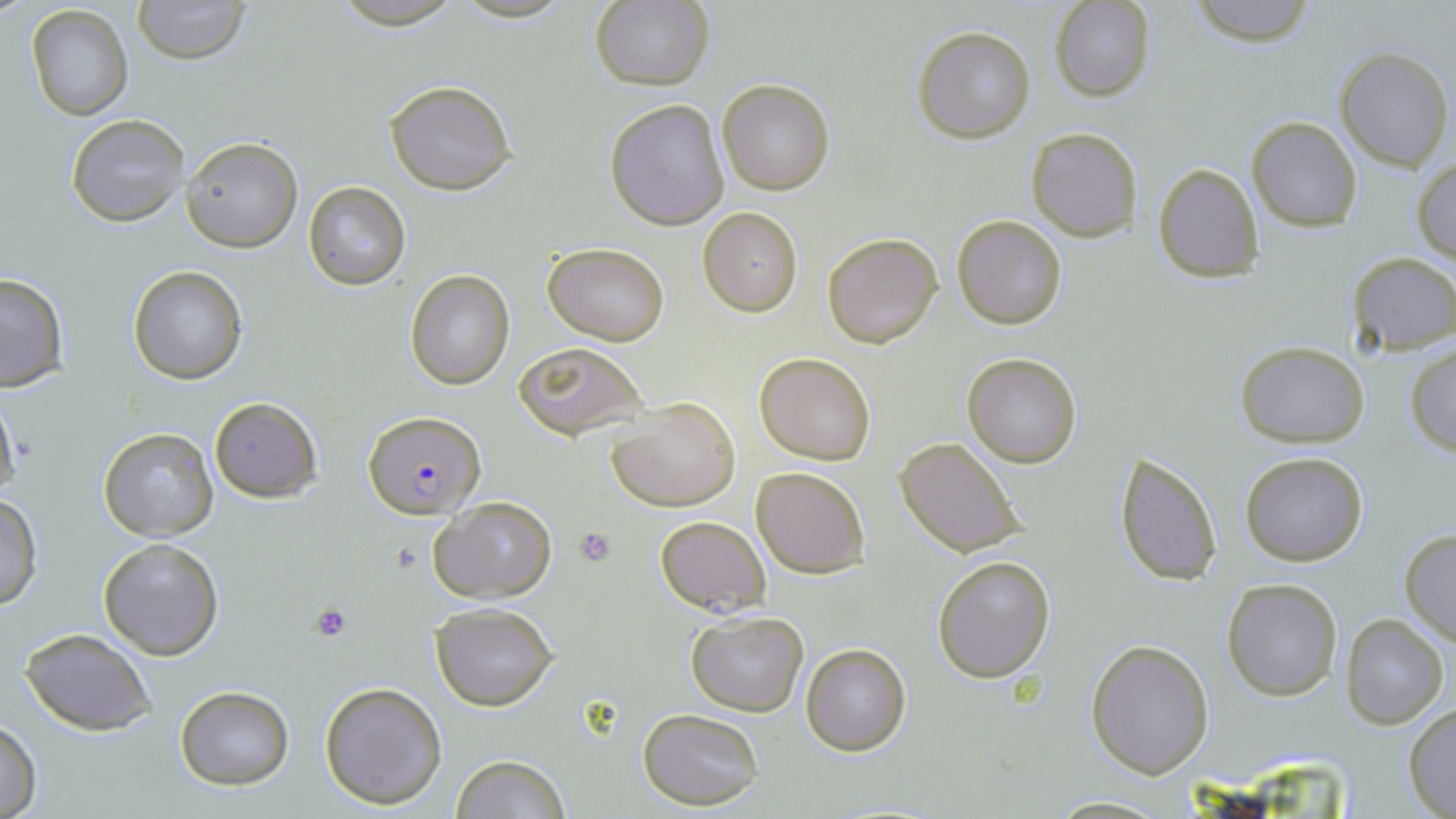

Summary:
  - Coordinate format: approximate bounding boxes as (x1,y1)-(x2,y2) corner pairs in pixels
  - Plasmodium falciparum-infected red blood cell locations: (362,410)-(483,518)
  - Platelet locations: (575,526)-(616,566), (310,603)-(352,642)
  - Uninfected red blood cell locations: (131,0)-(251,64), (329,0)-(465,28), (590,0)-(714,91), (1188,0)-(1319,45), (1050,1)-(1155,102), (26,5)-(132,119), (913,26)-(1037,144), (1333,46)-(1453,171), (383,78)-(517,195), (715,78)-(836,196), (604,99)-(729,230), (66,113)-(188,227), (1246,116)-(1362,232), (1025,127)-(1143,242), (183,137)-(304,253), (1412,156)-(1456,266), (1153,163)-(1265,282), (303,181)-(411,289), (698,208)-(802,317), (952,215)-(1067,330), (822,232)-(943,348), (543,243)-(670,345), (1346,252)-(1456,354), (128,266)-(246,384), (405,270)-(515,389), (0,273)-(68,391), (1233,340)-(1371,447), (515,342)-(647,440), (1405,343)-(1456,456), (962,352)-(1083,468), (754,353)-(875,464), (0,390)-(22,504), (607,395)-(740,511), (208,397)-(322,501), (98,427)-(219,542), (894,435)-(1028,559), (1114,448)-(1223,586), (1239,452)-(1369,567), (750,465)-(870,578), (0,491)-(43,610), (428,497)-(558,604), (656,515)-(770,617), (1399,528)-(1456,647), (98,537)-(225,659), (932,555)-(1054,682), (1221,578)-(1343,701), (430,603)-(559,711), (685,611)-(809,717), (1339,613)-(1449,729), (21,628)-(156,737), (1087,638)-(1215,778), (800,643)-(911,755), (319,680)-(449,810), (174,686)-(294,789), (1404,703)-(1456,816), (639,710)-(764,809), (0,718)-(42,817), (450,753)-(570,819), (1046,796)-(1175,817)
  - Slide-level diagnosis: Plasmodium falciparum
  - Stain: May-Grünwald-Giemsa
  - Image size: 1456×819 pixels
  - Field of view: single
  - Magnification: 1000x
  - Modality: optical microscopy
  - Preparation: thin blood smear